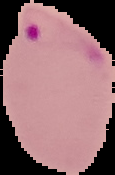
Summary:
  - Preparation: thin blood film
  - Image size: 115×175 pixels
  - Image type: cell region segmented out of the field of view; surrounding area masked to black
  - Malaria status: parasitized